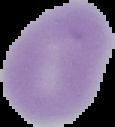

Cell region segmented out of the field of view; the surrounding area is masked to black. Image is 115×127 pixels. From a thin blood smear. Malaria status: uninfected.